Give the position of every leukocyte visible.
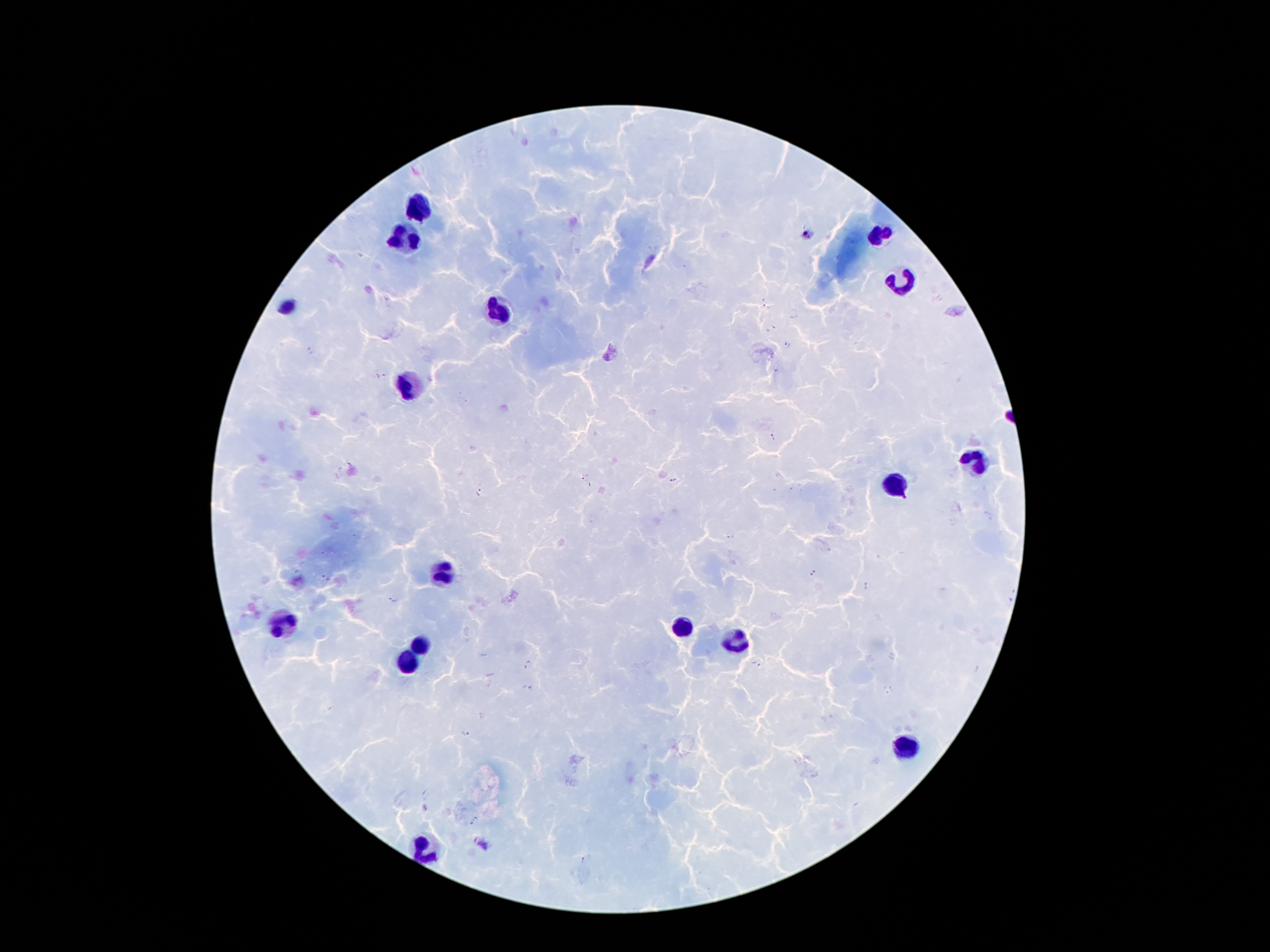
Approximate centers as [x, y] in pixels.
Leukocytes: [420, 211], [880, 234], [407, 238], [901, 280], [286, 307], [498, 309], [409, 385], [974, 465], [895, 483], [441, 572], [277, 624], [678, 628], [737, 641], [420, 645], [407, 666], [907, 748], [422, 851].

Summary:
  - Malaria parasite locations: [808, 235], [766, 307], [772, 328], [788, 343], [311, 350], [381, 376], [773, 438], [584, 478], [674, 480], [481, 492], [731, 537], [815, 573], [326, 579], [868, 587], [395, 600], [1010, 600], [529, 664], [755, 666], [528, 688], [887, 689], [467, 732], [475, 821], [481, 844], [585, 859]
  - Capture: smartphone through the microscope eyepiece
  - Patient malaria status: positive for Plasmodium falciparum
  - Stain: Giemsa
  - Preparation: thick blood smear
  - Magnification: 100x
  - Image size: 1270×952 pixels
  - Field of view: single